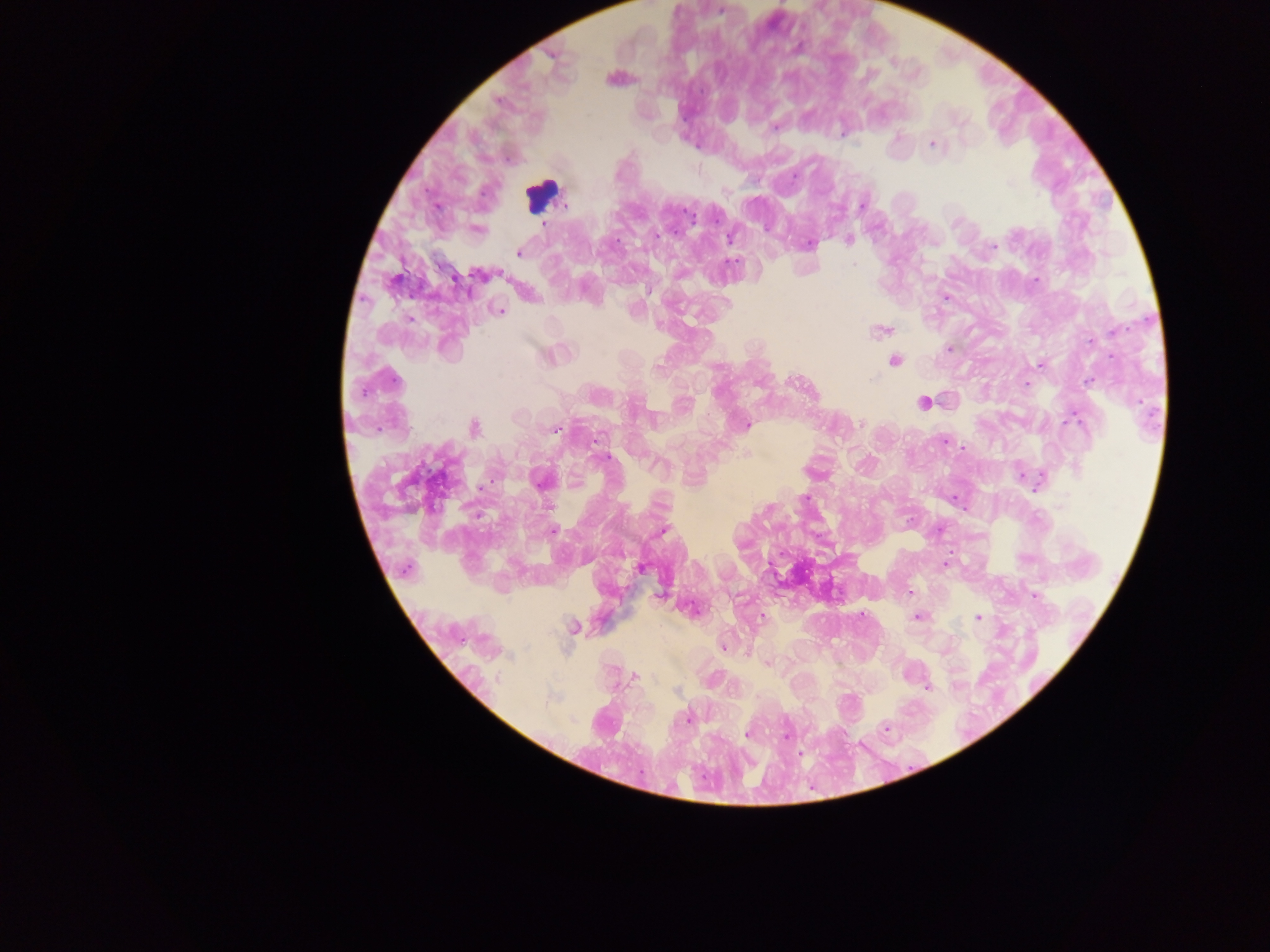 Approximate centers as [x, y] in pixels. Leukocyte locations: [541, 195]. Plasmodium parasite locations: [613, 78], [896, 138], [933, 144], [862, 205], [544, 224], [475, 229], [730, 237], [848, 239], [810, 243], [519, 251], [480, 274], [1034, 280], [945, 296], [498, 310], [881, 330], [949, 348], [549, 354], [893, 361], [1040, 364], [1026, 385], [923, 402], [861, 423], [746, 425], [473, 428], [555, 429], [943, 439], [963, 448], [747, 454], [605, 457], [1020, 475], [541, 480], [1039, 481], [954, 498], [939, 529], [664, 530], [551, 532], [944, 564], [640, 567], [909, 592], [661, 594], [1035, 596], [691, 609], [761, 616], [860, 616], [917, 617], [979, 617], [572, 627], [723, 646], [766, 662], [634, 676], [927, 687], [676, 690], [688, 718], [885, 728], [747, 735], [785, 737], [799, 753]. Thick blood film. Sample from Ghana. Mobile-phone photograph taken through the microscope. One field of view. Image is 1270×952 pixels.